State the blood parasite species.
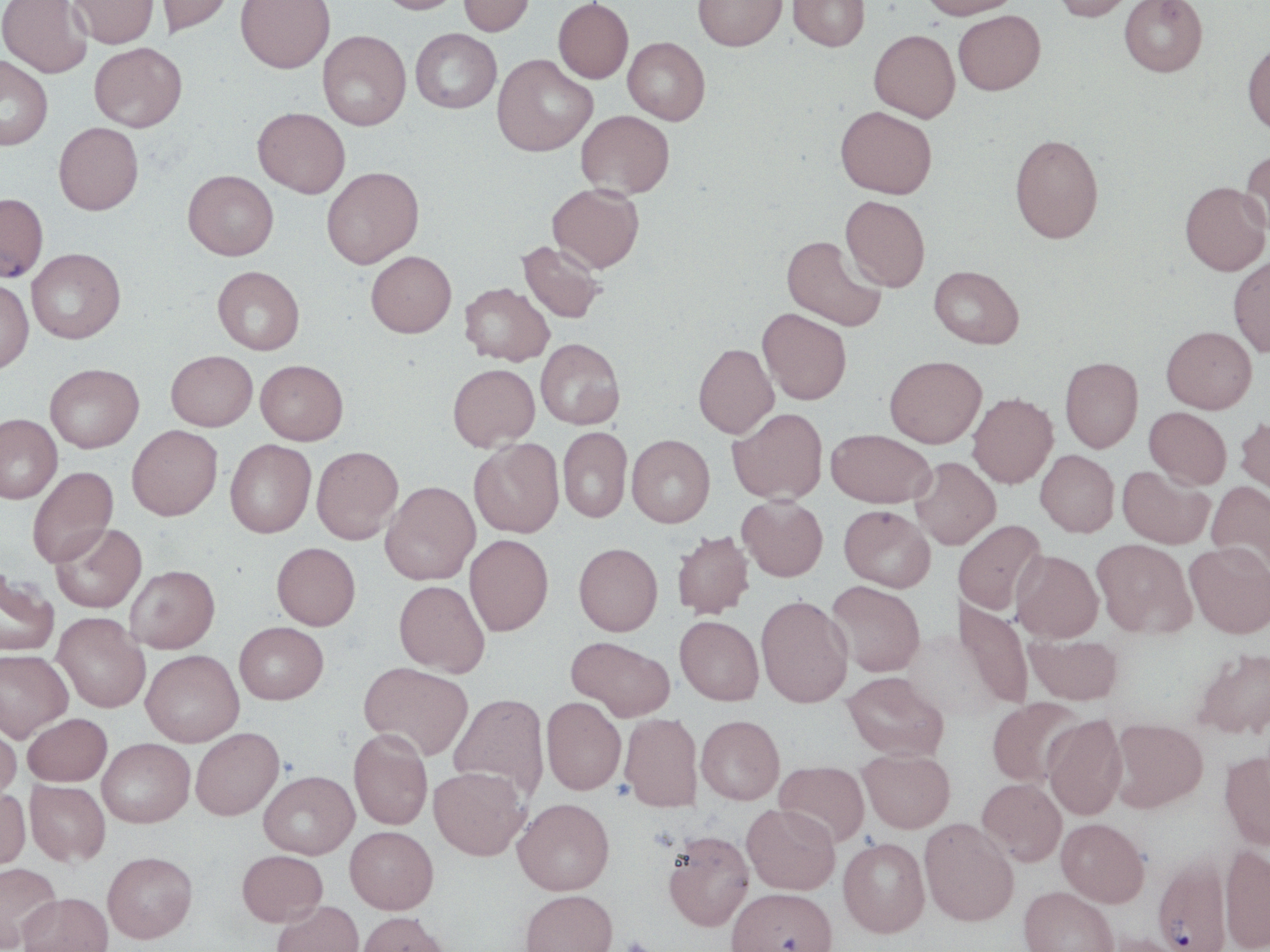

Plasmodium falciparum.

Approximate bounding boxes as [x1, y1, x2, y2] in pixels. Plasmodium falciparum-infected red blood cell locations: [0, 193, 49, 281], [1152, 852, 1232, 952]. Uninfected red blood cell locations: [0, 0, 93, 78], [69, 0, 159, 49], [155, 0, 235, 37], [235, 0, 335, 73], [374, 0, 464, 14], [458, 0, 535, 36], [553, 0, 633, 83], [693, 0, 787, 51], [788, 0, 870, 51], [919, 0, 1021, 19], [1051, 0, 1136, 21], [1119, 0, 1208, 77], [953, 10, 1045, 95], [410, 28, 502, 113], [869, 29, 960, 122], [318, 30, 411, 130], [623, 37, 710, 125], [1242, 41, 1270, 135], [90, 42, 187, 132], [492, 54, 597, 156], [0, 55, 53, 150], [835, 106, 937, 198], [253, 107, 350, 198], [576, 110, 674, 198], [54, 122, 144, 214], [1010, 134, 1104, 243], [1240, 148, 1270, 235], [321, 167, 424, 268], [183, 170, 278, 260], [1180, 181, 1269, 275], [547, 184, 644, 272], [840, 195, 931, 291], [782, 235, 886, 331], [518, 240, 606, 323], [27, 248, 125, 343], [366, 251, 456, 337], [1229, 255, 1270, 357], [929, 265, 1024, 348], [212, 266, 304, 355], [0, 277, 34, 373], [460, 282, 554, 365], [758, 308, 852, 404], [1162, 326, 1256, 413], [536, 338, 625, 429], [693, 343, 778, 438], [166, 350, 257, 430], [884, 355, 987, 447], [1060, 356, 1143, 452], [256, 360, 348, 444], [45, 363, 144, 452], [448, 363, 539, 451], [967, 393, 1058, 488], [1144, 407, 1232, 489], [728, 408, 827, 504], [0, 414, 62, 503], [1234, 416, 1270, 502], [127, 425, 223, 520], [558, 426, 632, 523], [826, 428, 935, 508], [627, 435, 715, 527], [225, 439, 316, 538], [469, 439, 564, 538], [312, 446, 403, 544], [1036, 450, 1119, 537], [910, 457, 1000, 549], [1119, 465, 1214, 549], [27, 467, 118, 568], [1206, 480, 1270, 576], [381, 481, 480, 585], [737, 495, 828, 581], [839, 505, 935, 592], [953, 519, 1046, 614], [50, 523, 146, 613], [671, 531, 754, 618], [465, 534, 554, 636], [1092, 539, 1197, 638], [271, 542, 361, 630], [574, 542, 663, 635], [1185, 542, 1270, 638], [1011, 550, 1103, 642], [125, 565, 220, 653], [0, 569, 60, 656], [394, 580, 489, 677], [827, 581, 925, 676], [756, 594, 853, 707], [953, 597, 1034, 710], [53, 613, 150, 712], [674, 615, 764, 705], [234, 622, 328, 704], [1025, 632, 1123, 705], [566, 636, 675, 720], [1192, 647, 1270, 740], [0, 649, 73, 741], [141, 649, 244, 746], [359, 662, 473, 760], [841, 672, 949, 761], [449, 692, 550, 801], [541, 697, 626, 794], [986, 697, 1086, 787], [23, 713, 112, 786], [620, 713, 702, 811], [1042, 713, 1128, 820], [696, 715, 784, 804], [0, 717, 21, 802], [1110, 718, 1208, 811], [191, 728, 284, 819], [349, 728, 433, 830], [98, 738, 195, 827], [857, 748, 955, 833], [1219, 750, 1270, 852], [775, 760, 870, 846], [429, 766, 528, 860], [259, 770, 359, 858], [976, 777, 1066, 866], [25, 779, 110, 866], [0, 788, 30, 869], [513, 797, 614, 895], [742, 803, 840, 894], [919, 818, 1019, 926], [1056, 818, 1150, 906], [344, 826, 439, 914], [663, 830, 754, 931], [838, 837, 930, 938], [1219, 843, 1270, 952], [237, 850, 327, 926], [102, 851, 197, 943], [0, 862, 61, 951], [1018, 886, 1118, 952], [727, 887, 839, 952], [520, 889, 617, 952], [19, 892, 113, 952], [272, 900, 364, 952], [357, 911, 450, 952], [1102, 932, 1192, 952]. Light microscopy. Thin blood film. May-Grünwald-Giemsa stain. Image is 1270×952 pixels. 1000x magnification. Single field of view.